Give the position of every Plasmodium parasite visible.
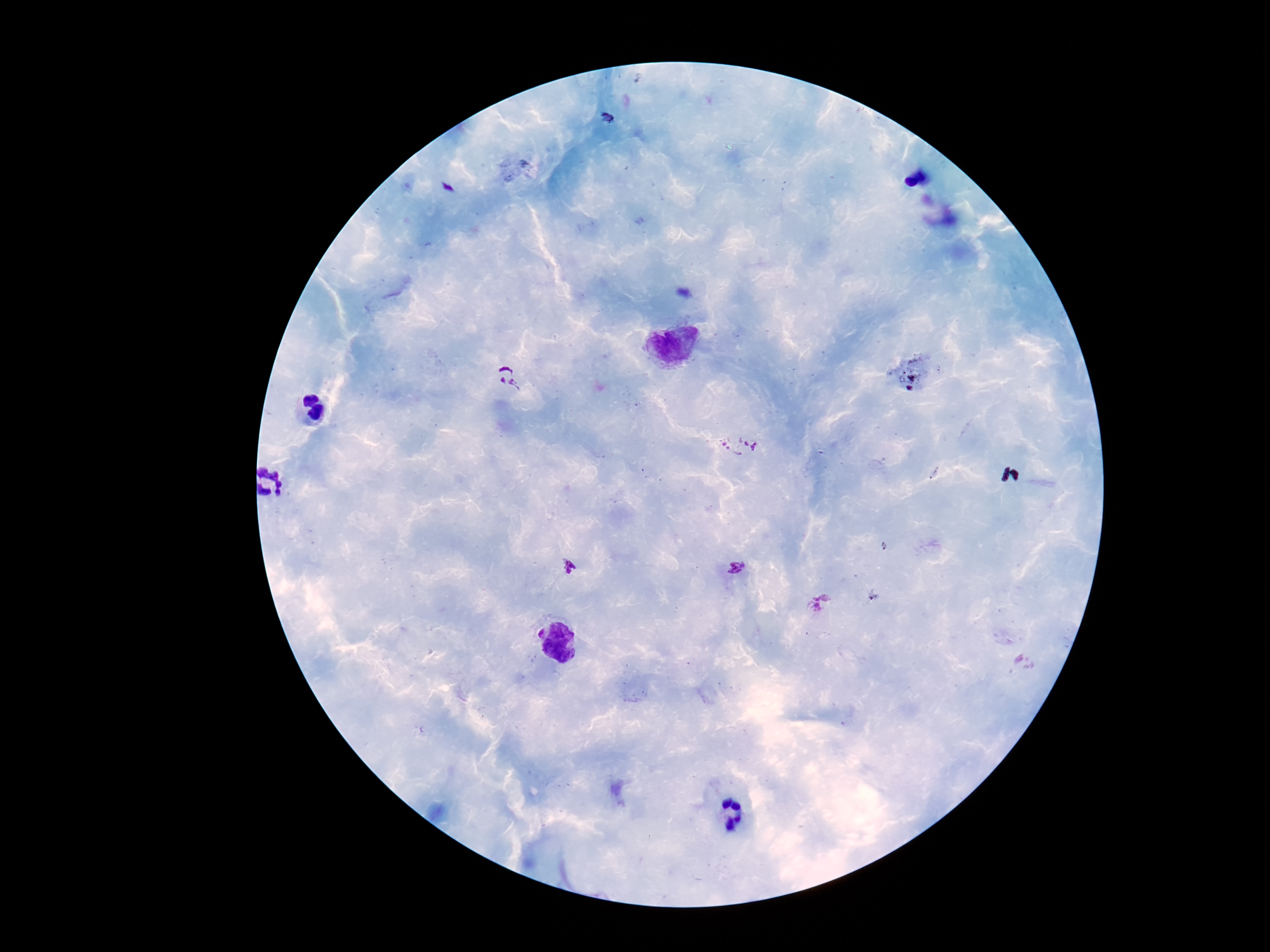

Approximate centers as (x, y) in pixels.
Plasmodium parasites: (507, 377), (738, 446), (569, 567), (737, 568), (817, 607).

field of view = one from this slide
magnification = 100x
preparation = thick blood film
image size = 1270×952 pixels
patient malaria status = positive
capture = smartphone camera through the microscope eyepiece
stain = Giemsa